Locate every Babesia divergens-infected red blood cell.
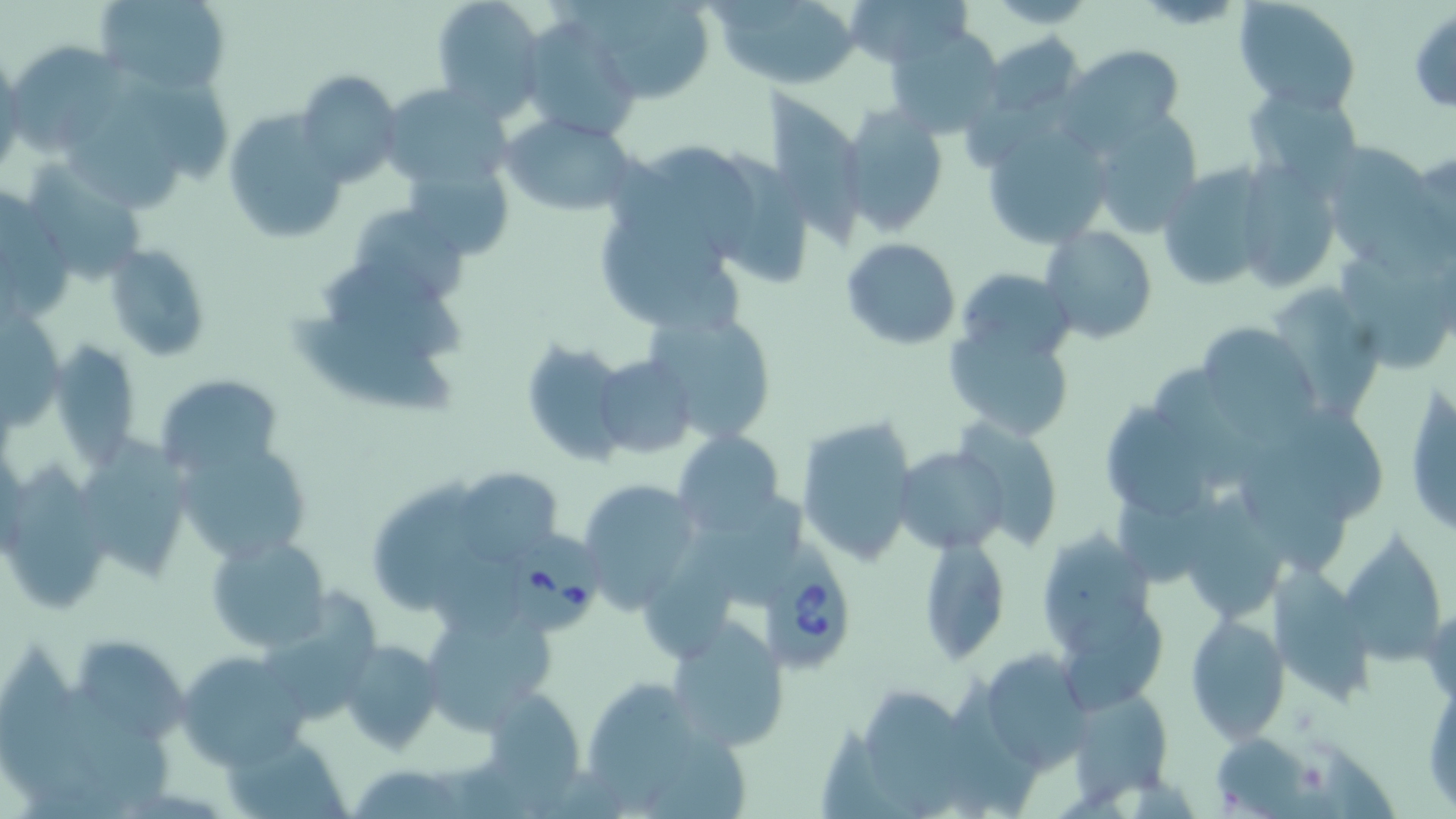
Approximate bounding boxes as (x1, y1, x2, y2) in pixels.
Babesia divergens-infected red blood cells: (508, 531, 599, 630), (755, 536, 853, 674).

{
  "slide_level_diagnosis": "Babesia divergens",
  "preparation": "thin blood film",
  "field_of_view": "one of a larger specimen",
  "uninfected_red_blood_cell_locations": "approximate bounding boxes as (x1, y1, x2, y2) in pixels: (95, 0, 231, 91), (431, 0, 548, 114), (583, 0, 714, 103), (840, 0, 967, 67), (984, 0, 1097, 28), (1234, 1, 1362, 114), (720, 3, 855, 87), (1408, 10, 1456, 112), (517, 16, 641, 143), (884, 27, 1007, 140), (978, 32, 1087, 126), (13, 44, 123, 158), (1061, 44, 1185, 147), (297, 71, 403, 187), (128, 74, 235, 172), (379, 83, 514, 189), (60, 84, 183, 212), (764, 84, 858, 246), (1243, 85, 1362, 189), (837, 105, 948, 234), (1083, 108, 1208, 234), (220, 109, 347, 245), (501, 113, 635, 216), (980, 119, 1113, 250), (650, 143, 758, 258), (1318, 146, 1439, 263), (1404, 146, 1456, 256), (725, 149, 808, 288), (614, 155, 723, 287), (406, 160, 514, 263), (22, 161, 143, 284), (1157, 164, 1275, 292), (1234, 165, 1344, 296), (0, 189, 71, 318), (355, 208, 471, 300), (602, 225, 742, 325), (1040, 226, 1156, 345), (841, 237, 960, 351), (105, 244, 211, 363), (1343, 256, 1450, 366), (312, 267, 468, 357), (963, 271, 1080, 355), (1273, 289, 1376, 417), (0, 309, 66, 431), (647, 310, 778, 445), (289, 316, 458, 412), (943, 318, 1076, 441), (1195, 322, 1319, 437), (55, 341, 135, 468), (519, 341, 627, 464), (595, 355, 697, 457), (1155, 369, 1268, 486), (154, 373, 284, 478), (1405, 380, 1454, 536), (1105, 395, 1206, 524), (1287, 411, 1385, 518), (794, 415, 919, 567), (959, 424, 1058, 551), (674, 431, 786, 536), (89, 434, 190, 585), (177, 439, 310, 566), (896, 447, 1010, 554), (1248, 461, 1341, 572), (1, 464, 112, 615), (463, 474, 560, 562), (577, 477, 701, 612), (370, 480, 471, 611), (1194, 493, 1280, 613), (1119, 497, 1222, 583), (718, 500, 804, 603), (1042, 520, 1156, 660), (1334, 532, 1449, 668), (205, 533, 332, 652), (919, 537, 1009, 664), (652, 539, 738, 658), (426, 557, 522, 636), (1275, 568, 1368, 702), (262, 590, 381, 718), (424, 604, 554, 732), (1184, 613, 1291, 743), (1062, 616, 1164, 722), (666, 618, 789, 751), (72, 636, 190, 743), (0, 638, 92, 800), (337, 638, 442, 753), (176, 650, 312, 771), (974, 650, 1093, 769), (1424, 676, 1455, 815), (955, 677, 1040, 817), (577, 678, 729, 814), (63, 683, 170, 793), (481, 686, 591, 806), (1064, 689, 1171, 802), (865, 690, 968, 819), (823, 724, 912, 819), (224, 732, 349, 819), (1211, 733, 1316, 817), (350, 763, 473, 818)",
  "modality": "optical microscopy",
  "magnification": "1000x",
  "stain": "May-Grünwald-Giemsa",
  "image_size": "1456×819 pixels"
}